Identify the parasite.
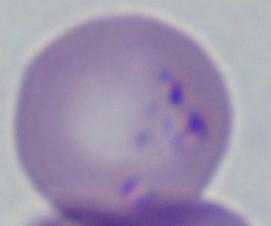

Babesia.

modality = micrograph
magnification = 1000x